Locate every P. falciparum parasite and give its life-cycle stage, and locate every leukocyte and any debris.
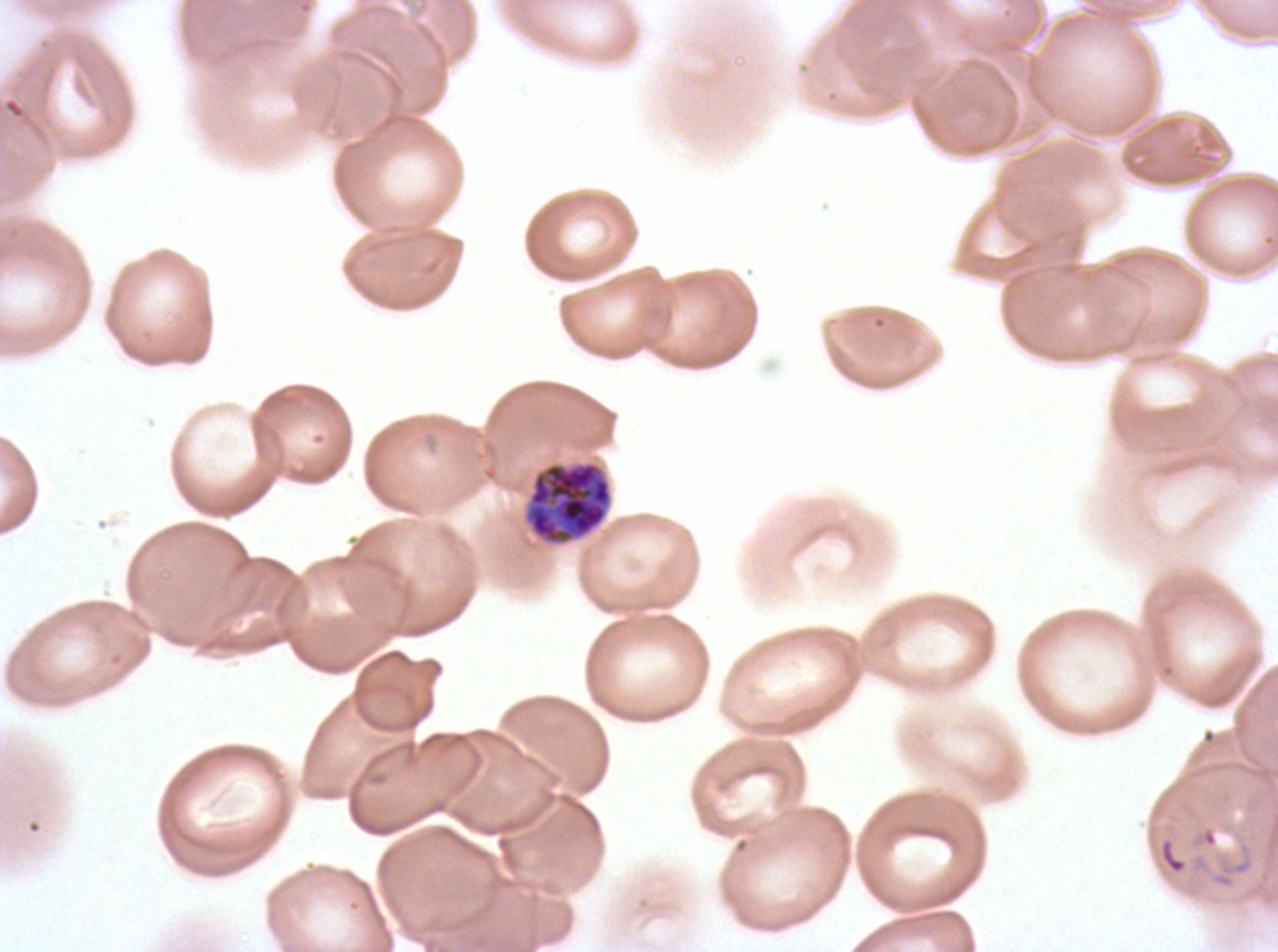

Approximate bounding boxes as [x1, y1, x2, y2] in pixels.
Rings: [1161, 841, 1186, 873].
Early schizonts: [528, 462, 611, 543].
No late-ring/early-trophozoite forms, mid trophozoites, late trophozoites, late schizonts, segmenters, gametocytes, leukocytes, or debris observed.

stain = Giemsa
life-cycle stages observed = ring, early schizont
preparation = thin blood film
specimen = ex-vivo P. falciparum culture from a patient in The Gambia, grown for 24 to 48 hours
field of view = one sub-image of a larger composite
image size = 1278×952 pixels